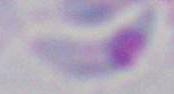
magnification = 1000x
modality = micrograph
identification = Toxoplasma gondii